Assess the morphology of the red blood cells.
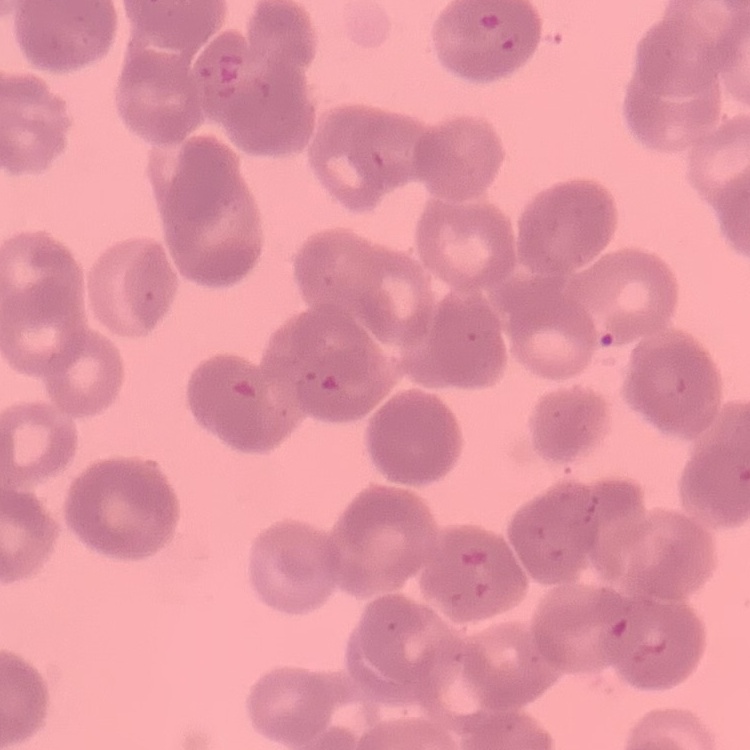

They show rouleaux formation.

{
  "preparation": "thin peripheral smear",
  "image_type": "one tile cut from a larger photomicrograph",
  "stain": "Field's or Giemsa"
}